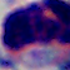 A leukocyte is shown. 1000x magnification. Photomicrograph.